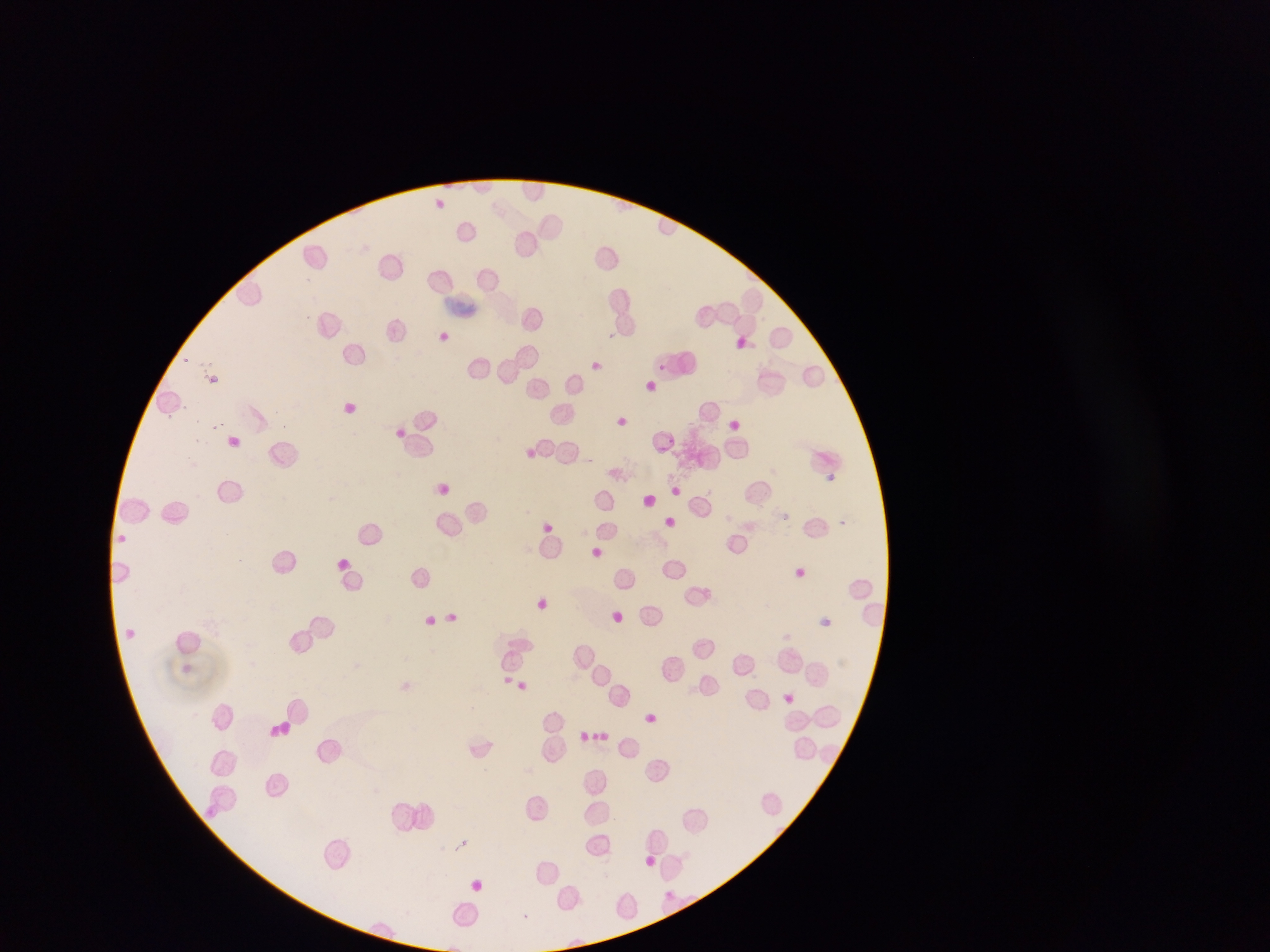 Approximate bounding boxes as left top right bottom in pixels. Malaria parasite locations: 182 357 191 366; 656 362 668 371; 730 419 739 429; 211 424 220 431; 826 474 834 482; 207 808 217 818; 666 889 674 899 | approximate x y pixel centers of objects too small to bound: 185 359. Artifact (stain precipitate or debris) locations: 450 291 481 322. Image is 1270×952 pixels. Mobile-phone photograph taken through the microscope. Sample from Ghana. Thin blood film. One field of view.